State the blood parasite species.
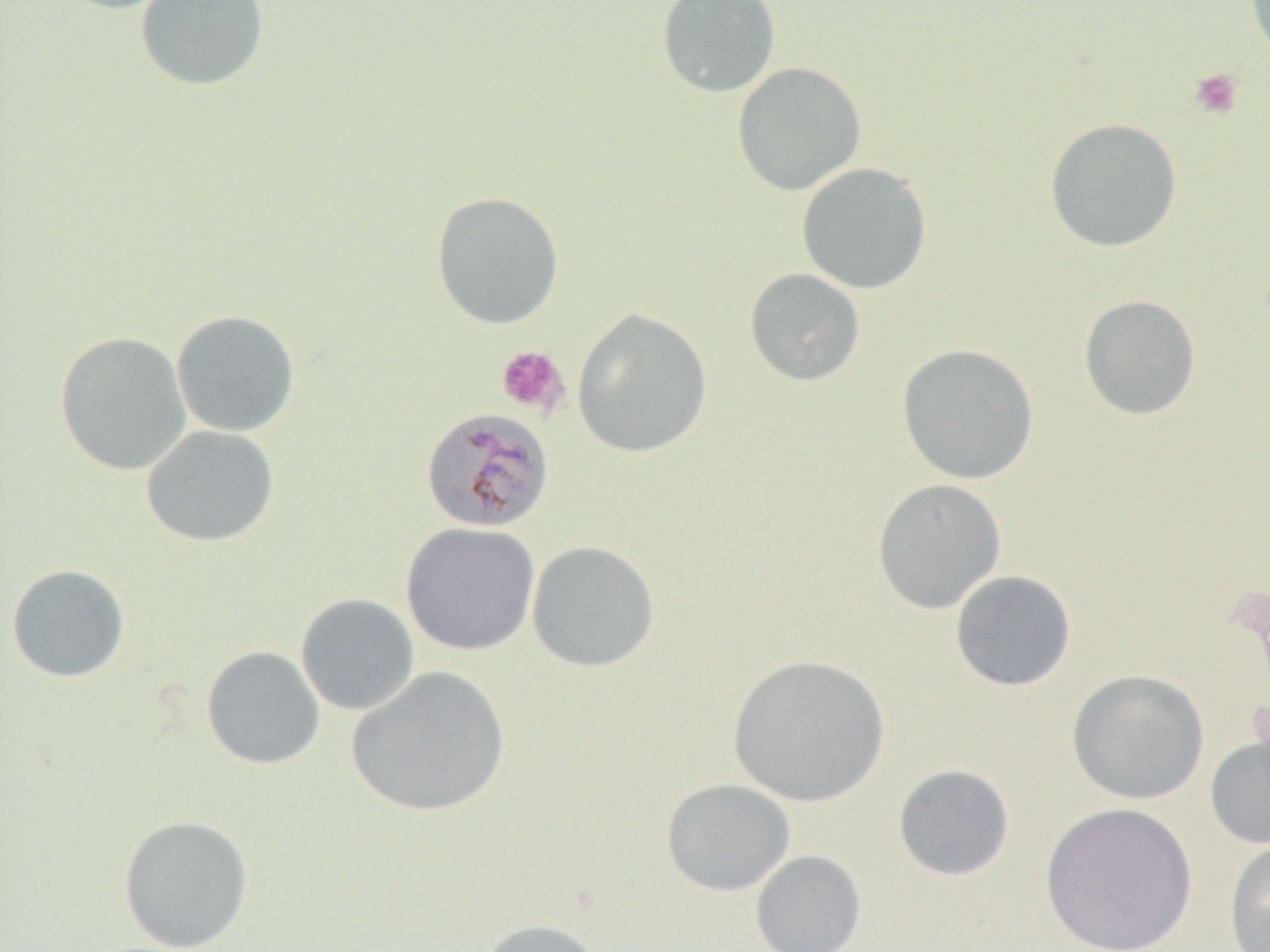

Plasmodium malariae.

image size = 1270×952 pixels
modality = light microscopy
platelet locations = approximate bounding boxes as (x1, y1, x2, y2) in pixels: (1188, 68, 1243, 119), (495, 345, 569, 416)
uninfected red blood cell locations = approximate bounding boxes as (x1, y1, x2, y2) in pixels: (52, 0, 184, 14), (136, 0, 269, 91), (657, 0, 781, 98), (1246, 0, 1270, 61), (732, 61, 867, 196), (1044, 117, 1183, 253), (796, 161, 932, 295), (430, 190, 566, 330), (744, 267, 866, 387), (1078, 294, 1202, 420), (571, 308, 713, 458), (170, 309, 302, 437), (54, 331, 192, 475), (896, 343, 1039, 484), (141, 424, 280, 548), (871, 478, 1007, 614), (400, 521, 540, 657), (526, 540, 661, 673), (6, 564, 131, 683), (949, 569, 1077, 692), (295, 593, 421, 716), (201, 645, 326, 771), (727, 653, 891, 808), (346, 666, 511, 818), (1067, 669, 1210, 804), (1204, 735, 1270, 849), (893, 764, 1016, 882), (661, 778, 796, 896), (1040, 802, 1198, 951), (117, 814, 255, 951), (1224, 838, 1270, 952), (750, 850, 867, 952), (477, 918, 608, 952)
magnification = 1000x
preparation = thin blood smear
field of view = single
Plasmodium malariae-infected red blood cell locations = approximate bounding boxes as (x1, y1, x2, y2) in pixels: (420, 406, 555, 533)